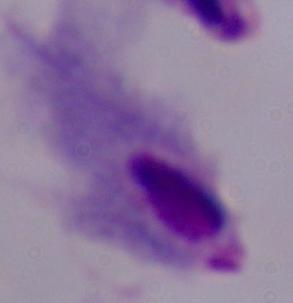

Captured at 1000x magnification. A trichomonad is shown. Micrograph.